Classify this cell by malaria status.
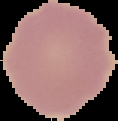
It is uninfected.

Summary:
  - Image size: 118×121 pixels
  - Preparation: thin blood film
  - Image type: cell region segmented out of the field of view; surrounding area masked to black